Name the blood parasite species.
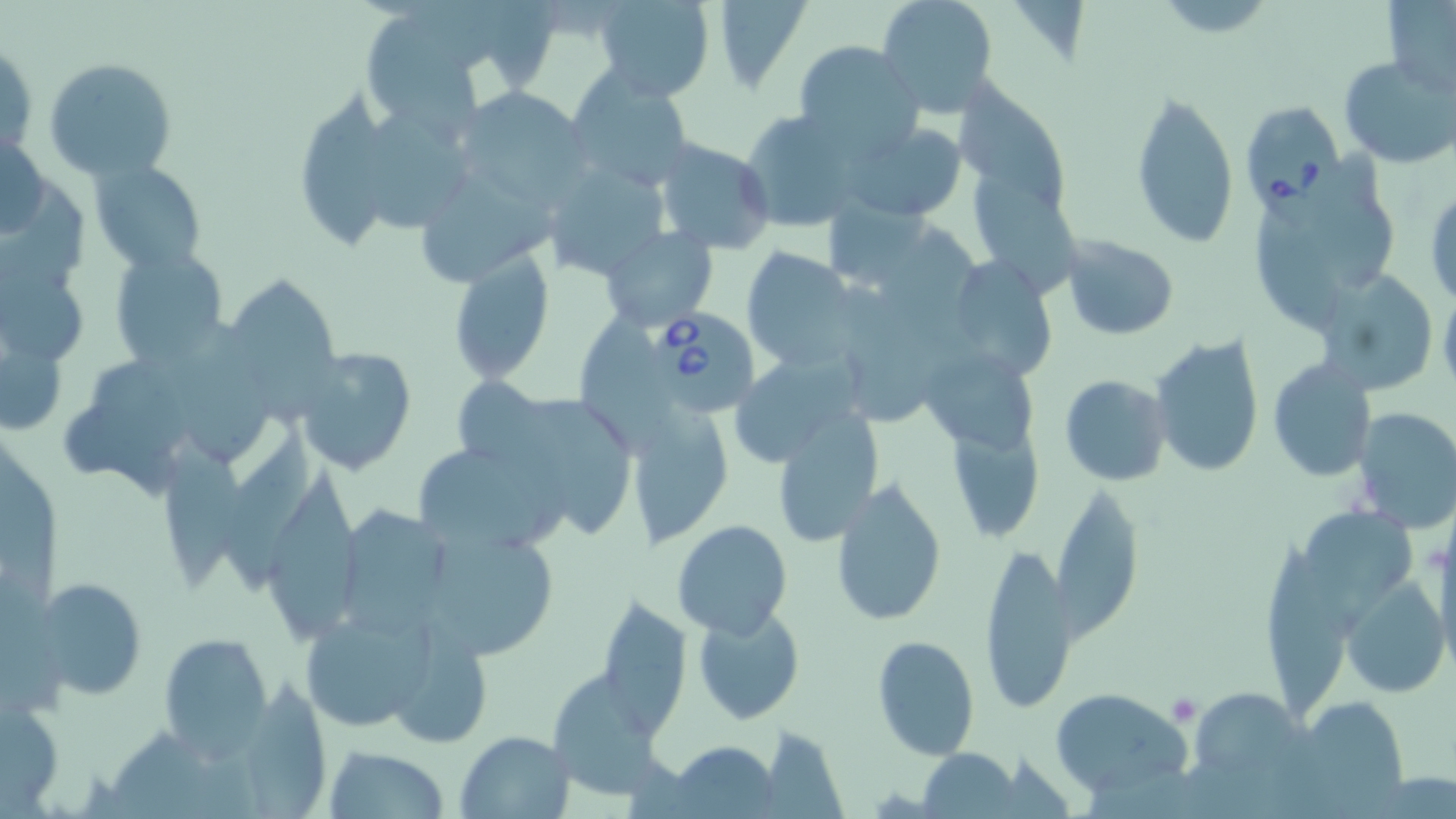

Babesia divergens.

Approximate bounding boxes as (x1,y1)-(x2,y2) corner pairs in pixels. Uninfected red blood cell locations: (477,0)-(564,95), (591,0)-(715,101), (709,0)-(811,91), (876,0)-(998,116), (1382,1)-(1456,99), (365,16)-(479,143), (1,37)-(37,160), (794,40)-(924,157), (1338,54)-(1455,169), (45,56)-(177,180), (565,72)-(696,191), (953,84)-(1067,209), (302,85)-(393,250), (452,89)-(594,207), (1129,89)-(1240,250), (739,108)-(866,231), (371,113)-(470,232), (842,123)-(968,223), (2,126)-(50,241), (653,137)-(777,256), (89,159)-(209,273), (542,159)-(669,278), (1247,166)-(1399,330), (965,173)-(1087,305), (422,180)-(565,286), (1425,186)-(1456,307), (829,199)-(929,283), (599,226)-(719,332), (1060,234)-(1179,340), (110,245)-(230,370), (740,246)-(861,371), (445,249)-(555,384), (954,254)-(1051,377), (0,263)-(93,365), (1312,269)-(1437,395), (232,277)-(343,429), (1439,282)-(1456,399), (836,283)-(932,424), (576,308)-(670,457), (179,320)-(275,466), (1151,336)-(1264,479), (296,345)-(419,476), (736,345)-(864,464), (924,345)-(1034,453), (1267,359)-(1376,482), (1059,375)-(1171,486), (457,377)-(556,462), (547,395)-(633,537), (621,399)-(733,547), (1350,406)-(1456,534), (773,407)-(883,547), (944,411)-(1042,540), (223,430)-(317,593), (164,436)-(243,587), (422,450)-(552,546), (260,462)-(358,645), (831,479)-(948,628), (1051,487)-(1144,645), (344,504)-(454,640), (672,520)-(793,639), (435,533)-(567,659), (1263,533)-(1348,723), (979,542)-(1076,715), (30,575)-(149,700), (1341,579)-(1450,699), (594,598)-(692,733), (692,603)-(805,725), (295,607)-(435,734), (402,628)-(492,746), (157,633)-(273,753), (872,635)-(980,759), (555,668)-(653,793), (246,682)-(326,819), (1048,687)-(1193,799), (1,695)-(66,814), (1291,696)-(1414,813), (759,727)-(846,817), (456,730)-(576,819), (667,740)-(779,817), (322,744)-(451,819), (919,748)-(1020,818). Babesia divergens-infected red blood cell locations: (1239,101)-(1345,210), (658,309)-(758,411). Platelet locations: (1168,693)-(1204,725). Single field of view. Image is 1456×819 pixels. Optical microscopy. May-Grünwald-Giemsa-stained preparation. Thin blood film. 1000x magnification.